Outline each uninfected red blood cell.
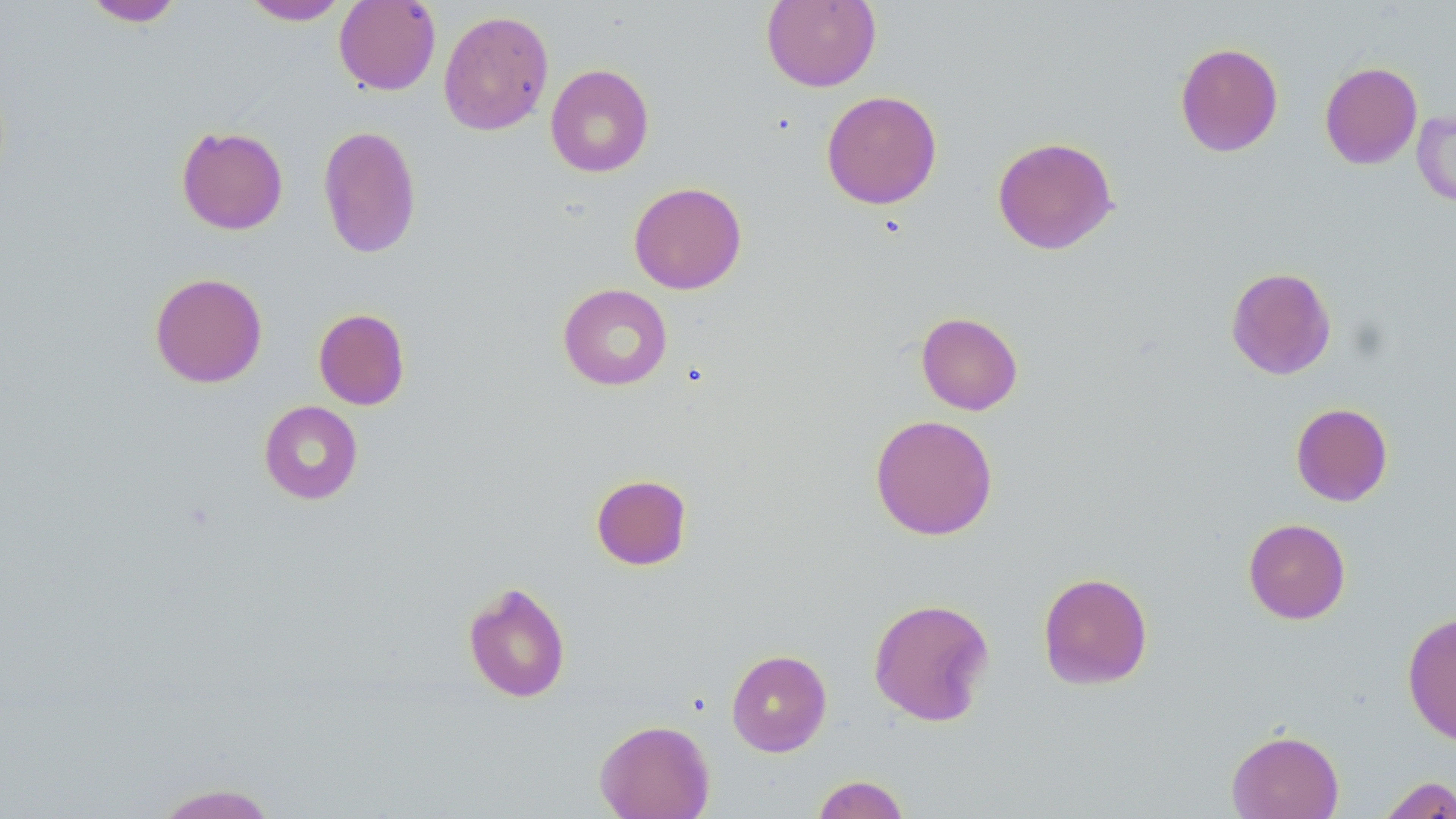

Approximate bounding boxes as (x1, y1, x2, y2) in pixels.
Uninfected red blood cells: (241, 0, 349, 25), (334, 0, 440, 95), (761, 0, 881, 92), (83, 1, 184, 27), (438, 9, 554, 136), (1174, 42, 1284, 157), (1319, 61, 1423, 169), (544, 64, 655, 178), (821, 90, 942, 209), (1412, 109, 1456, 209), (317, 125, 422, 259), (175, 126, 289, 235), (992, 136, 1118, 255), (628, 182, 747, 295), (1225, 266, 1337, 380), (149, 272, 268, 388), (558, 284, 672, 391), (313, 308, 410, 410), (916, 311, 1023, 415), (259, 400, 363, 505), (1290, 403, 1393, 506), (870, 414, 998, 541), (590, 473, 692, 571), (1243, 518, 1351, 624), (1037, 571, 1153, 690), (462, 581, 572, 703), (868, 597, 995, 727), (1402, 612, 1456, 746), (726, 649, 832, 757), (594, 719, 715, 819), (1226, 729, 1344, 819), (811, 775, 910, 819), (1377, 775, 1456, 818), (151, 782, 280, 818).

Summary:
  - Slide-level diagnosis: negative for blood parasites
  - Image size: 1456×819 pixels
  - Field of view: single
  - Modality: light microscopy
  - Magnification: 1000x
  - Stain: May-Grünwald-Giemsa
  - Preparation: thin blood smear